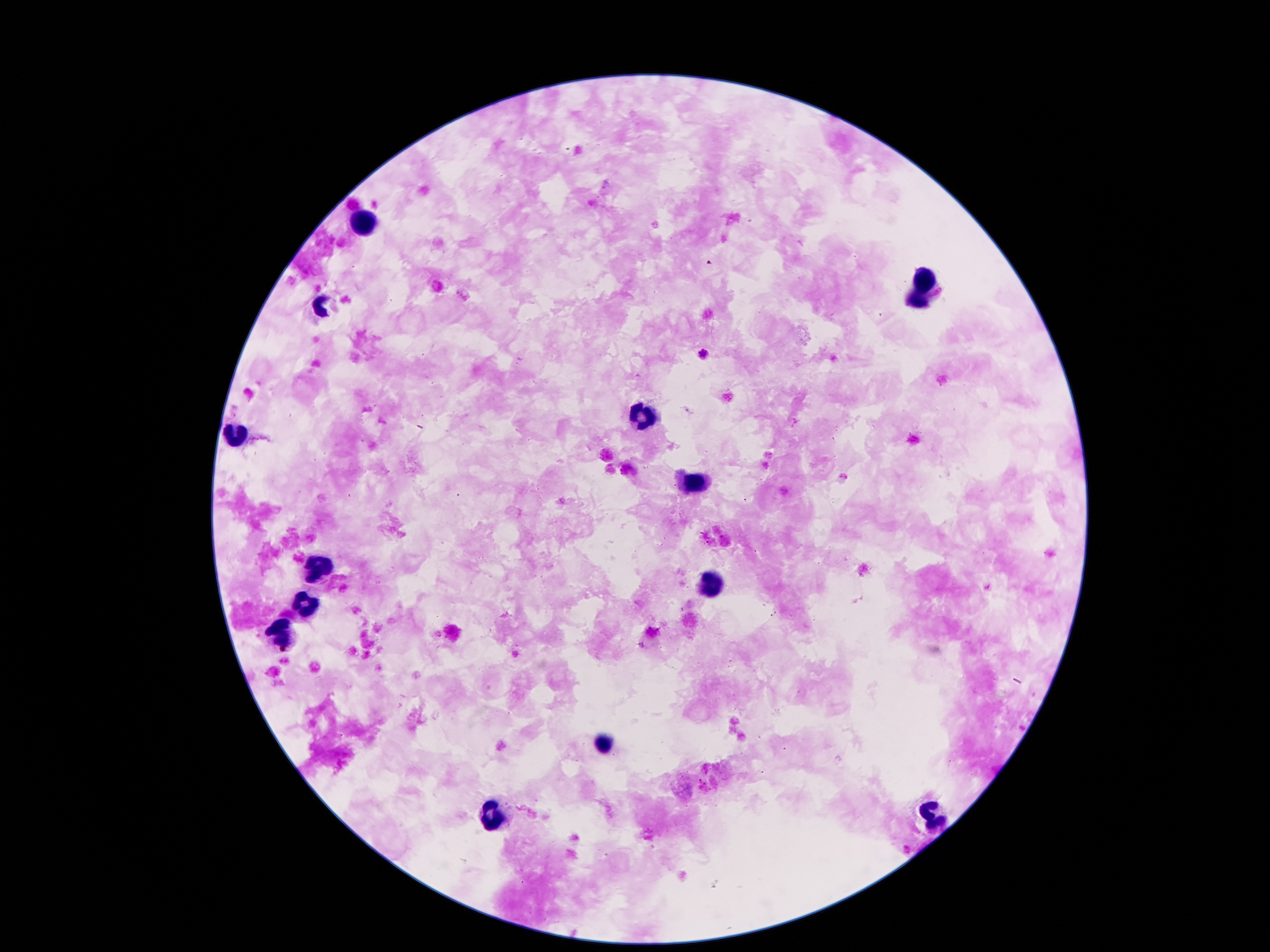

coordinate format = approximate centers as {x, y} in pixels
leukocyte locations = {361, 221}, {925, 275}, {915, 302}, {322, 309}, {641, 419}, {232, 434}, {691, 484}, {318, 567}, {714, 585}, {305, 606}, {282, 634}, {600, 742}, {930, 817}, {495, 819}
Plasmodium parasite locations = {709, 264}, {703, 354}
patient malaria status = positive for Plasmodium falciparum
preparation = thick peripheral-blood smear
field of view = single
stain = Giemsa
image size = 1270×952 pixels
magnification = 100x
capture = smartphone through the microscope eyepiece